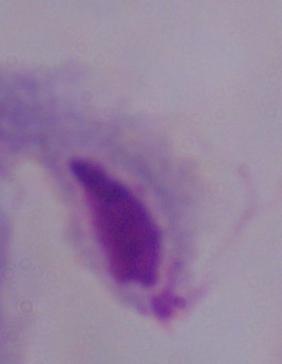

A trichomonad is seen. Micrograph. Captured at 1000x magnification.